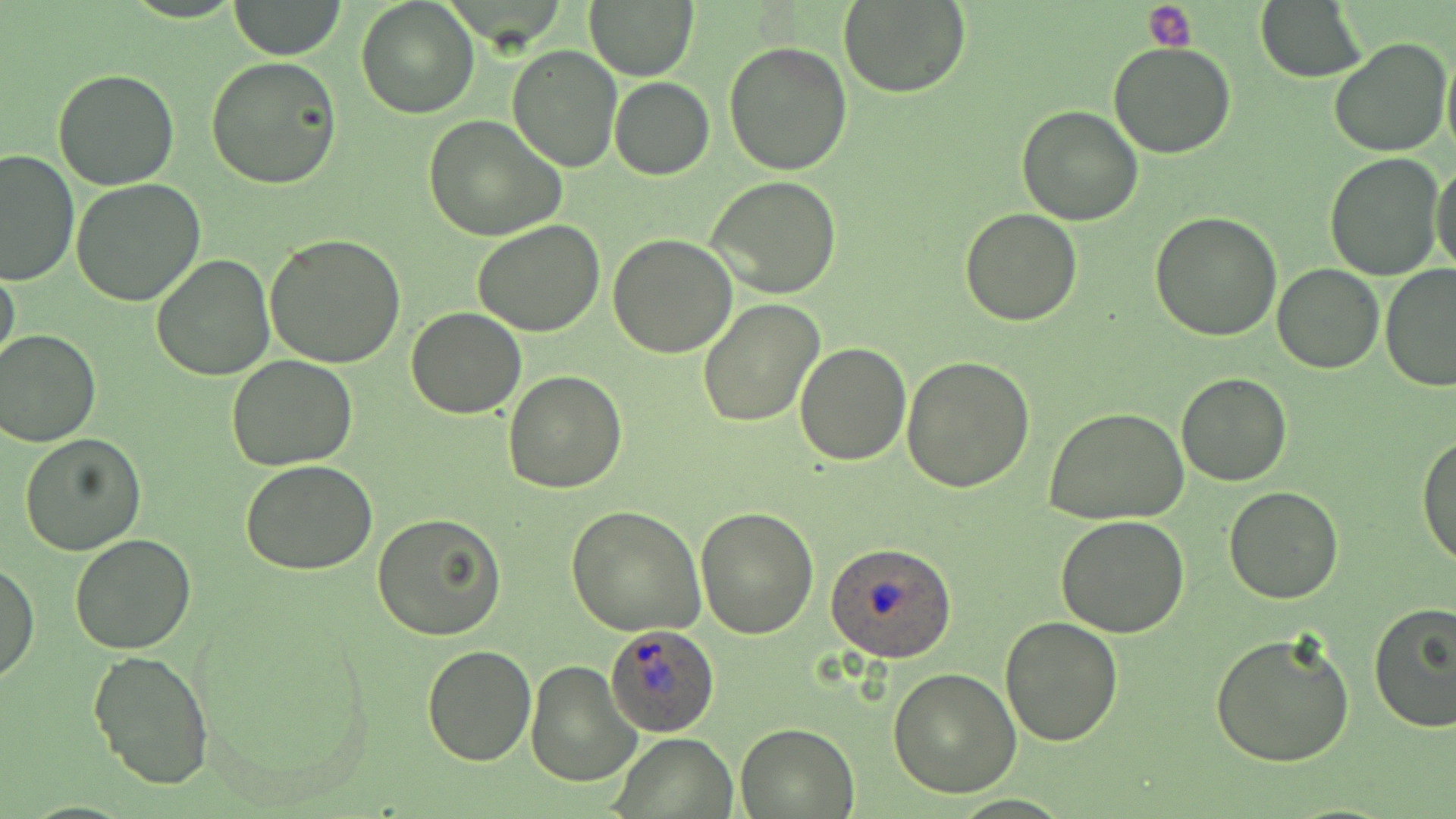
Summary:
  - Coordinate format: approximate bounding boxes as (x1,y1)-(x2,y2) corner pairs in pixels
  - Plasmodium ovale-infected red blood cell locations: (826,542)-(957,662), (603,622)-(721,737)
  - Platelet locations: (1142,4)-(1196,50)
  - Uninfected red blood cell locations: (355,0)-(480,119), (584,0)-(699,81), (1257,0)-(1369,83), (230,1)-(345,59), (837,1)-(970,98), (1329,35)-(1453,156), (724,40)-(854,177), (1108,43)-(1236,159), (1441,43)-(1456,164), (507,44)-(623,172), (206,56)-(342,190), (53,69)-(181,190), (610,76)-(714,181), (1016,104)-(1144,225), (424,115)-(569,242), (0,147)-(79,287), (1324,152)-(1446,281), (1430,159)-(1456,277), (706,176)-(842,299), (72,177)-(205,305), (959,208)-(1084,327), (1150,211)-(1281,339), (473,218)-(605,336), (264,233)-(408,370), (608,234)-(738,356), (151,253)-(275,379), (0,259)-(21,380), (1273,263)-(1384,375), (1379,264)-(1456,393), (697,299)-(824,428), (406,306)-(526,420), (0,327)-(101,447), (795,341)-(911,464), (227,355)-(359,472), (902,355)-(1036,492), (503,371)-(628,493), (1175,373)-(1292,486), (1044,407)-(1190,525), (20,432)-(147,555), (1417,432)-(1456,569), (240,460)-(378,576), (1225,486)-(1343,604), (696,504)-(819,639), (566,505)-(705,636), (373,510)-(507,642), (1056,517)-(1190,638), (69,534)-(196,655), (0,559)-(39,684), (1369,603)-(1456,737), (1001,615)-(1123,745), (1209,628)-(1356,770), (422,646)-(536,766), (89,648)-(214,789), (525,659)-(641,786), (888,666)-(1022,796), (735,723)-(857,817), (611,732)-(735,818)
  - Slide-level diagnosis: Plasmodium ovale
  - Field of view: one of a larger specimen
  - Magnification: 1000x
  - Modality: optical microscopy
  - Image size: 1456×819 pixels
  - Stain: May-Grünwald-Giemsa
  - Preparation: thin blood film